Assess the morphology of the erythrocytes.
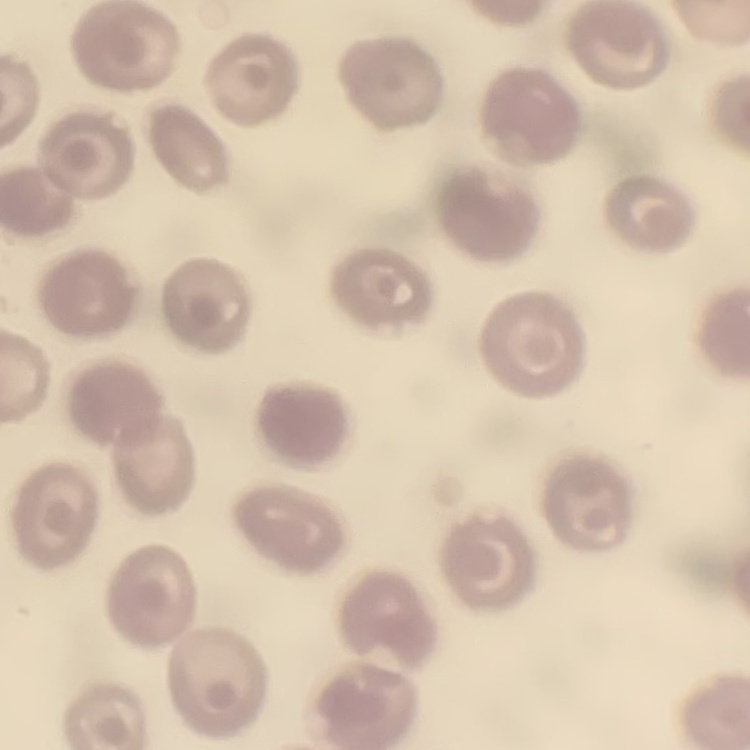
They show no rouleaux formation.

Summary:
  - Image type: square crop of a larger photomicrograph
  - Preparation: thin peripheral smear
  - Stain: Field's or Giemsa